Mark where platelets are.
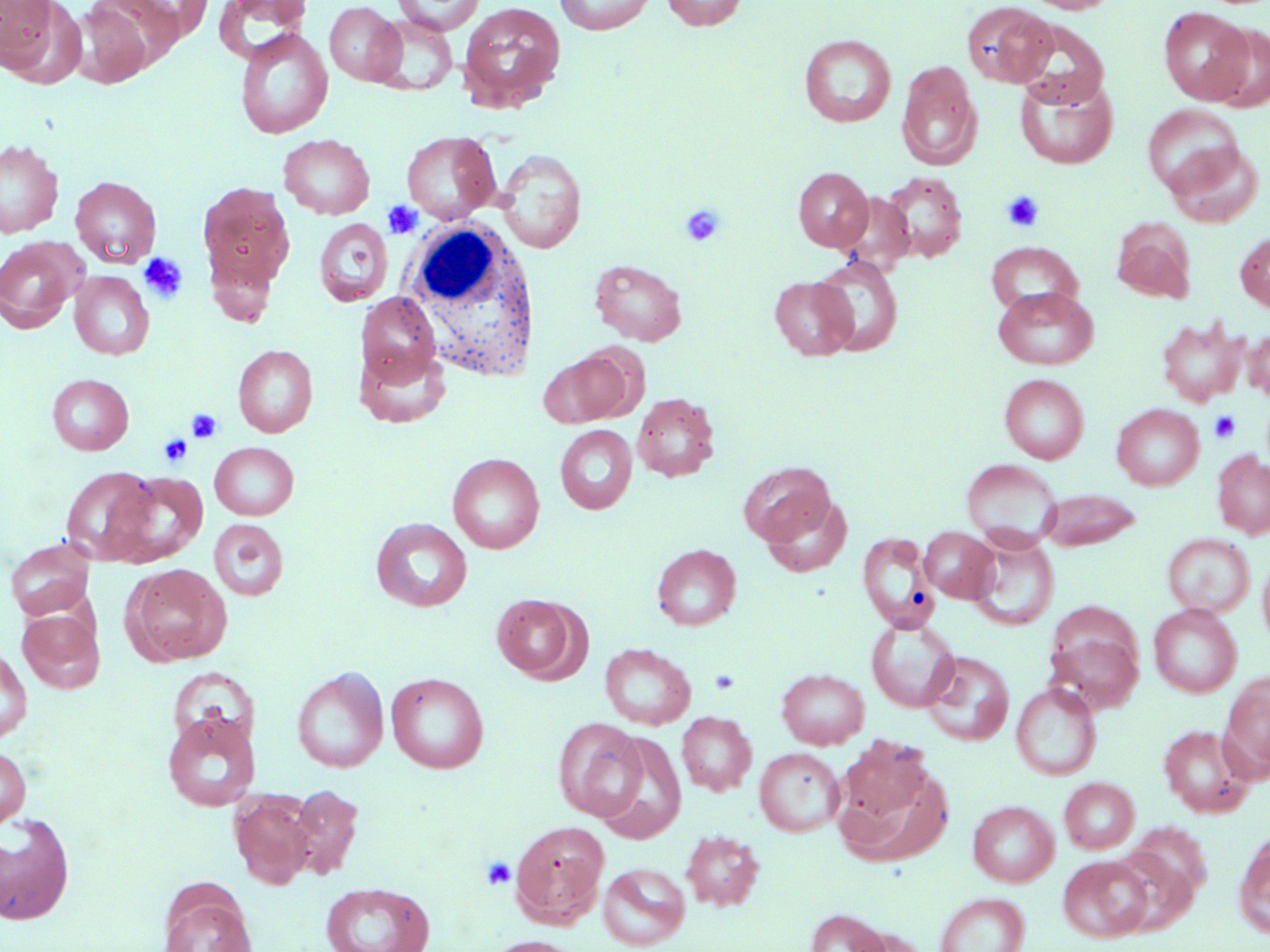
Approximate bounding boxes as (x1,y1)-(x2,y2) corner pairs in pixels.
Platelets: (1001,191)-(1045,233), (383,201)-(423,239), (680,203)-(725,246), (139,252)-(188,303), (186,408)-(223,442), (1209,410)-(1241,443), (159,434)-(192,467), (709,668)-(741,695), (481,856)-(517,889).

White blood cell locations: (399,221)-(544,384). Uninfected red blood cell locations: (0,0)-(84,87), (113,0)-(215,41), (214,0)-(312,62), (392,0)-(485,35), (554,0)-(657,35), (661,0)-(748,31), (1025,0)-(1117,14), (67,1)-(166,87), (961,1)-(1055,88), (324,2)-(405,86), (458,2)-(566,112), (1158,6)-(1252,104), (369,14)-(458,95), (1012,19)-(1109,108), (1206,23)-(1270,111), (234,28)-(333,139), (799,34)-(896,127), (896,61)-(982,170), (1015,74)-(1119,169), (1142,104)-(1243,196), (401,130)-(500,223), (279,134)-(375,219), (0,138)-(64,239), (1165,141)-(1263,227), (495,149)-(587,253), (794,167)-(874,251), (881,171)-(968,263), (70,176)-(161,268), (197,181)-(296,298), (1112,217)-(1197,303), (314,218)-(393,306), (1235,231)-(1270,316), (0,237)-(83,333), (986,241)-(1082,316), (812,256)-(903,356), (590,259)-(687,345), (69,271)-(154,360), (769,276)-(857,360), (993,286)-(1097,370), (356,292)-(441,384), (1157,317)-(1248,407), (1243,329)-(1270,402), (571,343)-(649,422), (233,344)-(318,437), (355,346)-(450,428), (538,352)-(626,427), (999,373)-(1088,463), (47,374)-(134,454), (632,393)-(719,482), (1112,403)-(1204,490), (555,424)-(637,514), (209,442)-(299,520), (1213,450)-(1270,539), (448,452)-(544,554), (961,458)-(1060,547), (739,461)-(835,545), (60,465)-(159,566), (109,471)-(209,567), (1037,488)-(1142,550), (760,494)-(852,577), (371,517)-(473,612), (209,519)-(288,601), (920,526)-(998,602), (857,532)-(939,633), (1162,533)-(1255,618), (968,534)-(1059,630), (5,538)-(96,620), (652,543)-(741,630), (1258,553)-(1270,649), (122,563)-(232,666), (491,593)-(586,683), (1148,604)-(1242,697), (18,608)-(104,693), (866,617)-(959,712), (1044,618)-(1146,713), (599,643)-(696,729), (0,647)-(32,744), (922,651)-(1015,746), (167,667)-(257,748), (291,667)-(389,773), (777,668)-(869,749), (386,672)-(489,773), (1220,674)-(1270,781), (1011,682)-(1102,780), (162,711)-(260,811), (676,711)-(756,796), (552,717)-(647,821), (1158,724)-(1255,817), (594,731)-(687,844), (838,737)-(935,829), (0,745)-(31,828), (754,747)-(845,836), (835,761)-(953,868), (1059,777)-(1139,854), (286,784)-(364,881), (230,791)-(317,889), (967,800)-(1059,886), (0,812)-(75,925), (510,820)-(610,926), (1125,821)-(1211,905), (680,830)-(765,911), (1234,832)-(1270,940), (1111,846)-(1200,935), (1058,856)-(1153,942), (598,862)-(690,950), (320,882)-(435,952), (158,886)-(257,952), (935,892)-(1030,952), (804,908)-(892,952), (484,935)-(585,952). Slide-level diagnosis: no evidence of blood parasites. One field of a larger specimen. 1000x magnification. May-Grünwald-Giemsa-stained preparation. Light microscopy. Thin blood smear. Image is 1270×952 pixels.